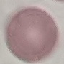

Summary:
  - Result: no malaria parasites seen
  - Stain: Giemsa
  - Capture: smartphone through the microscope eyepiece
  - Preparation: thin blood film
  - Image type: cell patch, automatically extracted from a larger field of view and resized to 64 × 64 pixels